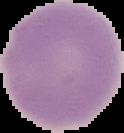

The area outside the segmented cell region is set to black. Result: no malaria parasites seen. From a thin blood smear. Image is 124×133 pixels.